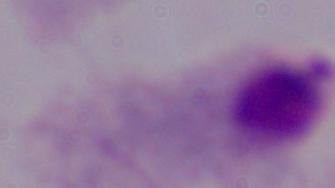

Summary:
  - Magnification: 1000x
  - Modality: photomicrograph
  - Identification: trichomonad